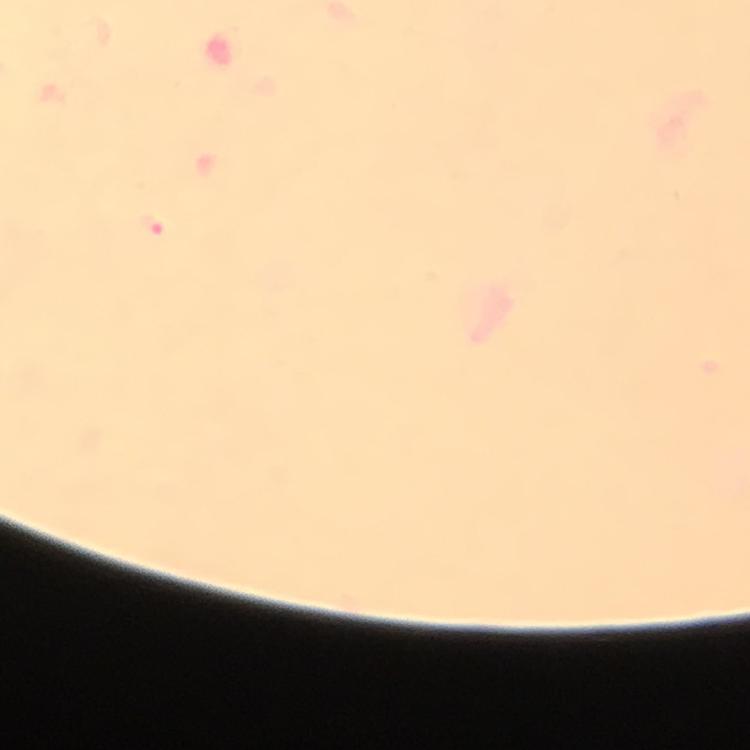
{
  "cropped_from": "one field of view",
  "context": "from a malaria diagnostic workup",
  "image_size": "750×750 pixels",
  "preparation": "thick smear",
  "magnification": "100x",
  "immersion_oil": "applied",
  "stain": "Giemsa",
  "malaria_parasite_locations": "approximate object centers, in pixels from the top-left corner: (x=148, y=226)",
  "capture": "smartphone photograph through a microscope"
}